Locate every leukocyte (white blood cell).
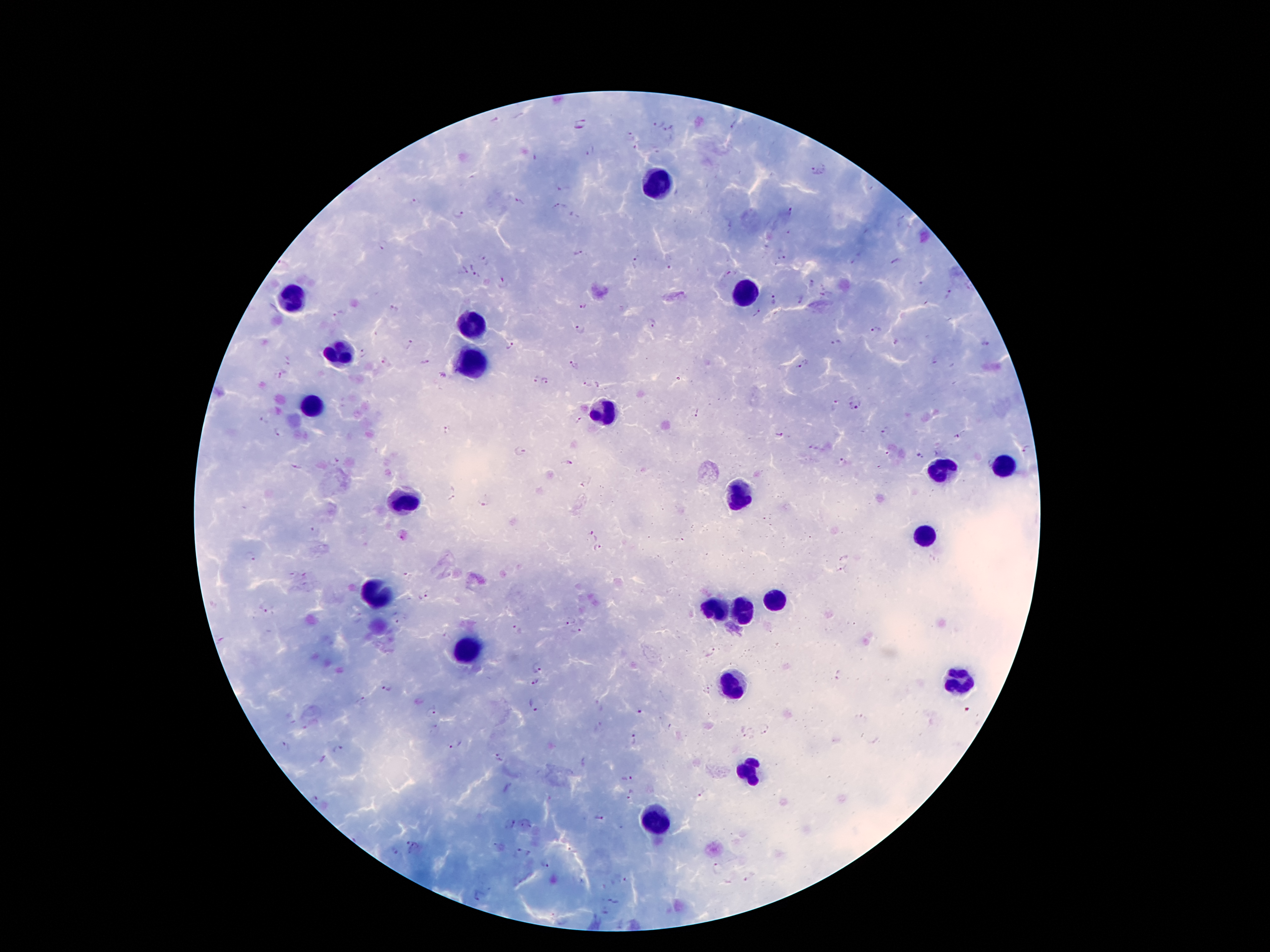

Approximate centers as {x, y} in pixels.
Leukocytes: {657, 182}, {745, 292}, {292, 298}, {471, 323}, {338, 355}, {471, 362}, {313, 405}, {606, 411}, {1003, 465}, {941, 469}, {733, 494}, {402, 499}, {929, 536}, {374, 594}, {774, 599}, {712, 607}, {741, 615}, {468, 650}, {959, 682}, {732, 686}, {749, 770}, {652, 817}.

malaria parasite locations = {495, 120}, {581, 124}, {657, 124}, {734, 125}, {669, 129}, {630, 136}, {590, 152}, {818, 169}, {414, 201}, {520, 202}, {556, 206}, {790, 212}, {458, 215}, {576, 216}, {383, 246}, {578, 253}, {783, 258}, {485, 259}, {635, 262}, {895, 262}, {283, 263}, {670, 268}, {463, 271}, {731, 272}, {476, 275}, {920, 281}, {504, 282}, {813, 282}, {949, 296}, {775, 299}, {800, 300}, {926, 303}, {582, 307}, {394, 309}, {758, 313}, {338, 314}, {653, 325}, {580, 329}, {874, 330}, {837, 343}, {896, 343}, {408, 345}, {511, 345}, {985, 345}, {363, 352}, {288, 359}, {382, 360}, {426, 363}, {573, 364}, {802, 365}, {282, 374}, {443, 375}, {535, 379}, {546, 382}, {587, 384}, {857, 407}, {836, 408}, {696, 413}, {262, 420}, {578, 420}, {448, 430}, {280, 431}, {885, 432}, {779, 434}, {959, 435}, {1027, 449}, {520, 451}, {887, 454}, {920, 456}, {335, 460}, {568, 462}, {989, 462}, {842, 463}, {294, 467}, {588, 485}, {452, 492}, {484, 502}, {311, 530}, {591, 536}, {598, 548}, {251, 555}, {844, 558}, {841, 570}, {290, 575}, {408, 577}, {422, 597}, {263, 608}, {398, 620}, {570, 621}, {517, 630}, {579, 632}, {223, 640}, {712, 653}, {539, 665}, {839, 676}, {535, 683}, {387, 687}, {707, 690}, {361, 699}, {597, 704}, {534, 705}, {640, 710}, {430, 712}, {861, 718}, {305, 728}, {434, 729}, {765, 729}, {747, 737}, {634, 740}, {456, 744}, {284, 747}, {338, 750}, {497, 756}, {585, 763}, {626, 777}, {632, 794}, {702, 794}, {315, 799}, {599, 818}, {510, 823}, {526, 824}, {413, 846}, {396, 851}, {518, 851}, {528, 853}, {545, 864}, {717, 869}, {750, 877}, {626, 879}, {480, 895}, {614, 900}, {605, 912}
stain = Giemsa
preparation = thick blood film
patient malaria status = positive for Plasmodium falciparum
magnification = 100x
capture = smartphone camera through the microscope eyepiece
field of view = single
image size = 1270×952 pixels